Locate every leukocyte (white blood cell).
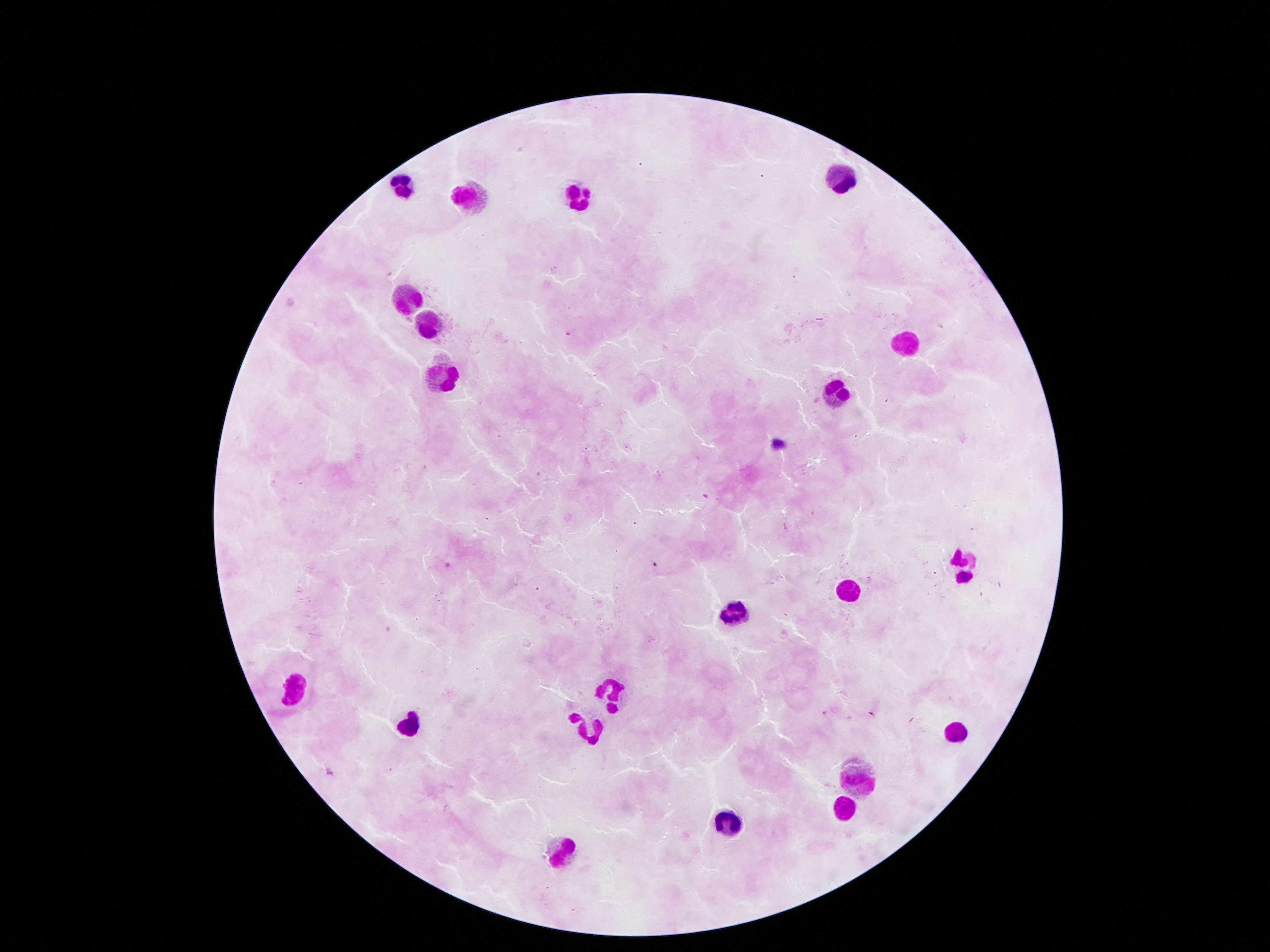
Approximate centers as [x, y] in pixels.
Leukocytes: [841, 178], [398, 185], [465, 191], [575, 192], [404, 290], [430, 319], [906, 341], [447, 372], [839, 390], [964, 564], [847, 587], [736, 607], [291, 685], [611, 695], [403, 719], [586, 725], [957, 729], [855, 776], [841, 806], [725, 815], [567, 849].

{
  "patient_malaria_status": "not infected",
  "image_size": "1270×952 pixels",
  "capture": "smartphone camera through the microscope eyepiece",
  "preparation": "thick blood smear",
  "field_of_view": "single",
  "magnification": "100x",
  "stain": "Giemsa"
}